Identify the preparation type.
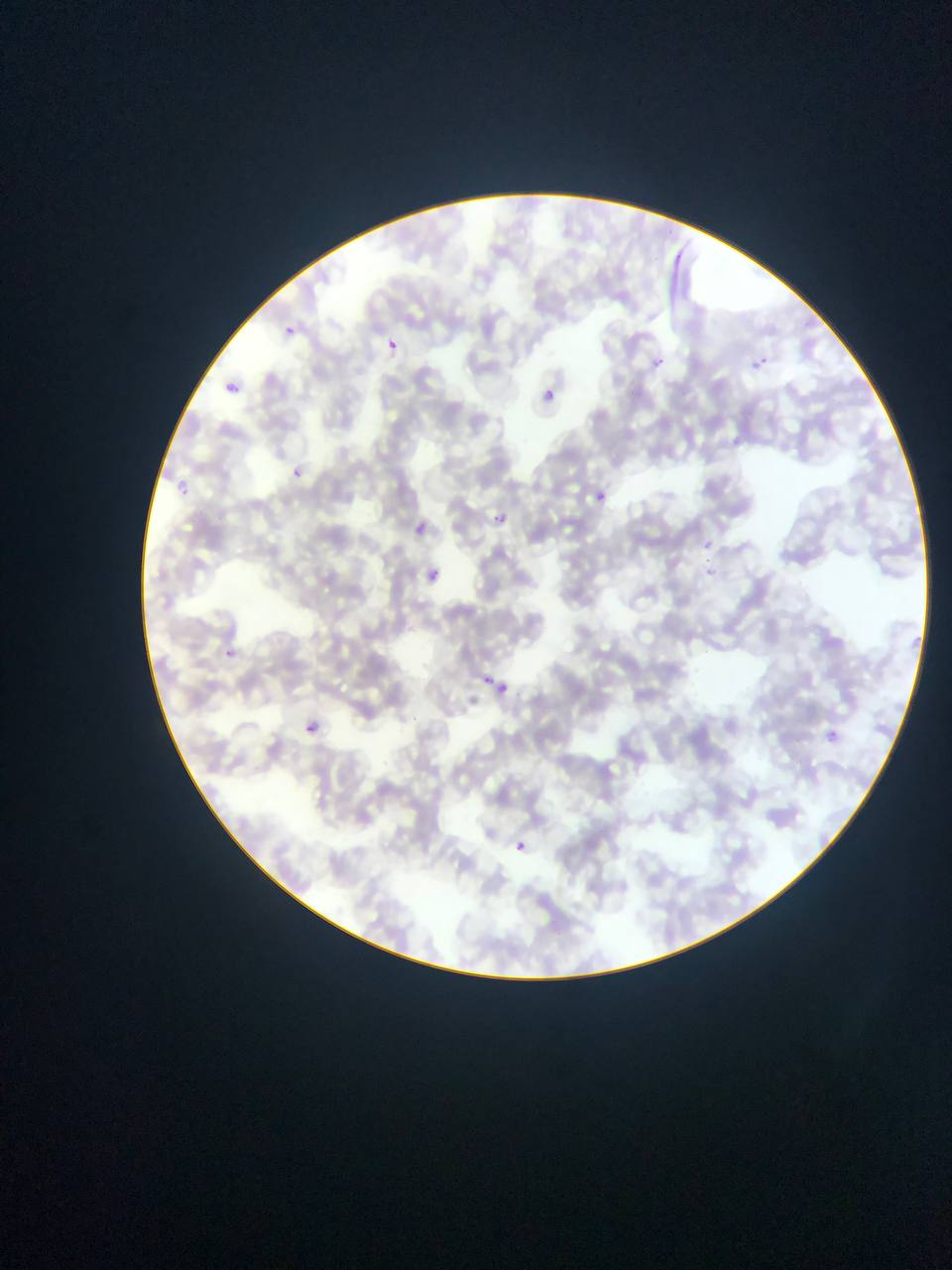
This is a thin smear.

Approximate bounding boxes as {left, top, right, bottom} in pixels. Plasmodium parasite locations: {281, 327, 292, 340}, {382, 339, 405, 353}, {653, 356, 672, 371}, {765, 356, 776, 368}, {751, 360, 762, 371}, {220, 383, 239, 396}, {542, 390, 560, 400}, {288, 467, 300, 479}, {174, 481, 192, 493}, {596, 491, 607, 503}, {492, 513, 507, 525}, {414, 521, 429, 536}, {700, 542, 713, 551}, {702, 559, 717, 575}, {428, 567, 442, 580}, {223, 647, 234, 660}, {484, 675, 494, 684}, {499, 677, 511, 694}, {305, 722, 319, 734}, {827, 730, 838, 741}, {515, 841, 526, 851}. Single field of view. Photographed through a microscope with a mobile-phone camera. Sample from Ghana. Image is 952×1270 pixels.